Outline each uninfected red blood cell.
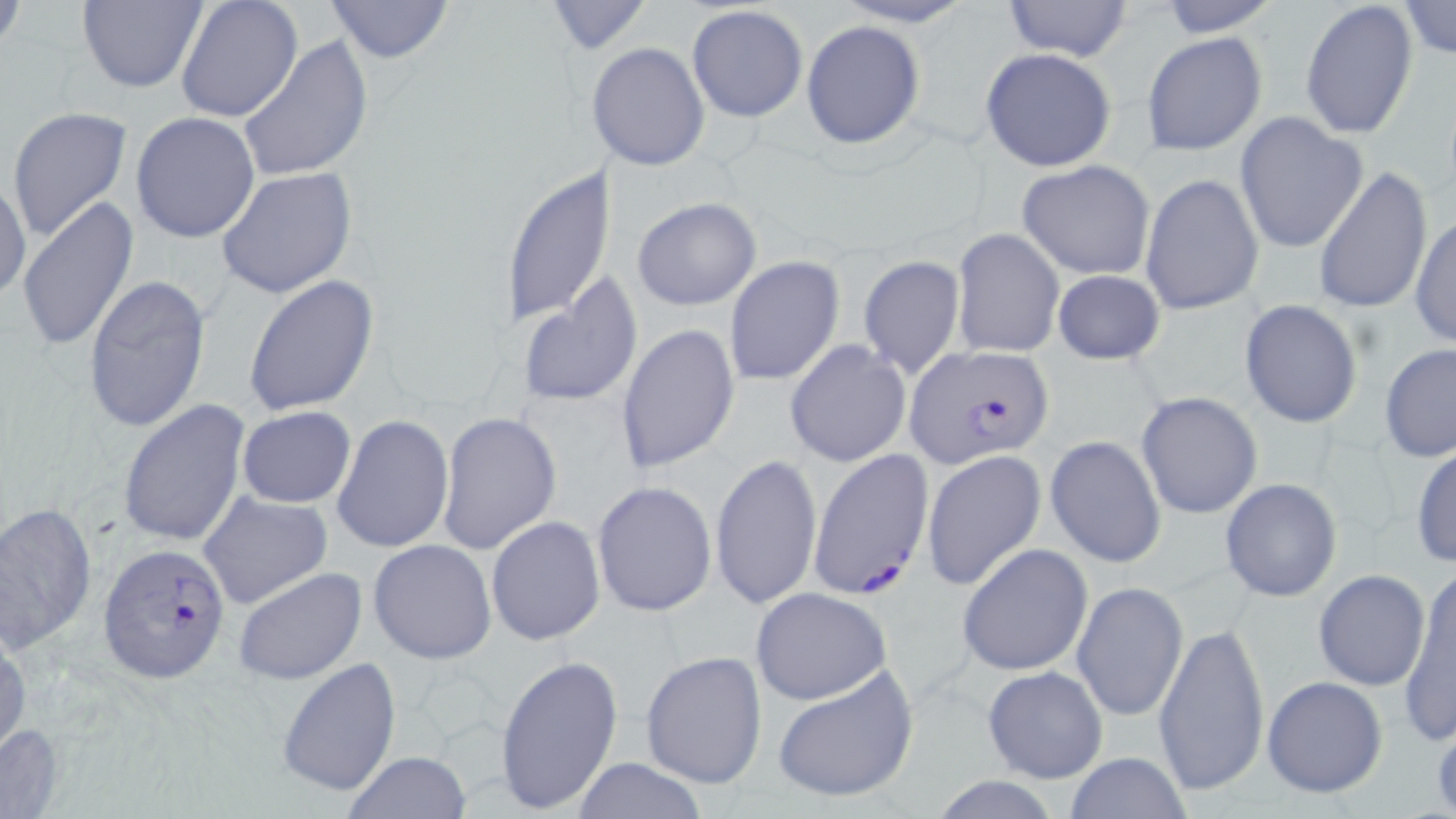

Approximate bounding boxes as [x1, y1, x2, y2] in pixels.
Uninfected red blood cells: [176, 0, 303, 123], [326, 0, 455, 65], [828, 0, 980, 28], [1001, 0, 1132, 64], [1155, 0, 1285, 35], [1299, 0, 1417, 142], [75, 1, 207, 93], [1398, 1, 1456, 60], [540, 2, 653, 54], [685, 4, 808, 124], [802, 20, 925, 149], [1141, 31, 1267, 157], [237, 35, 373, 183], [595, 42, 710, 172], [979, 47, 1118, 172], [6, 106, 132, 243], [131, 112, 260, 242], [1235, 112, 1370, 253], [1016, 160, 1156, 279], [499, 165, 613, 328], [1312, 165, 1433, 316], [215, 166, 358, 301], [1140, 173, 1264, 316], [1, 176, 30, 306], [16, 196, 139, 353], [632, 197, 761, 310], [1410, 214, 1455, 348], [951, 228, 1064, 359], [858, 255, 966, 382], [724, 257, 844, 387], [1051, 269, 1165, 365], [82, 273, 212, 436], [517, 273, 643, 412], [245, 275, 380, 417], [1239, 300, 1362, 429], [617, 324, 738, 475], [784, 340, 911, 468], [1379, 343, 1456, 462], [1136, 391, 1263, 520], [119, 400, 250, 548], [237, 406, 356, 509], [220, 408, 353, 598], [438, 411, 562, 556], [333, 414, 454, 555], [1045, 436, 1167, 568], [1411, 444, 1456, 567], [922, 450, 1046, 590], [710, 451, 822, 612], [1218, 478, 1343, 602], [592, 480, 718, 618], [198, 490, 332, 609], [0, 500, 96, 653], [486, 515, 605, 646], [368, 539, 497, 664], [957, 543, 1093, 676], [231, 566, 367, 686], [1312, 569, 1431, 690], [1397, 571, 1456, 746], [1071, 580, 1189, 722], [751, 587, 891, 706], [1154, 618, 1269, 800], [0, 626, 29, 762], [1158, 648, 1389, 794], [639, 649, 767, 787], [495, 651, 622, 816], [277, 657, 400, 798], [770, 663, 920, 804], [981, 665, 1109, 783], [1262, 675, 1387, 798], [0, 722, 64, 819], [1063, 751, 1193, 819], [344, 752, 470, 819], [570, 757, 707, 819], [928, 775, 1065, 818].

{
  "slide_level_diagnosis": "Plasmodium falciparum",
  "stain": "May-Grünwald-Giemsa",
  "image_size": "1456×819 pixels",
  "magnification": "1000x",
  "plasmodium_falciparum_infected_red_blood_cell_locations": "approximate bounding boxes as [x1, y1, x2, y2] in pixels: [903, 343, 1055, 468], [808, 449, 934, 602], [100, 542, 234, 680]",
  "preparation": "thin blood smear",
  "field_of_view": "single",
  "modality": "light microscopy"
}